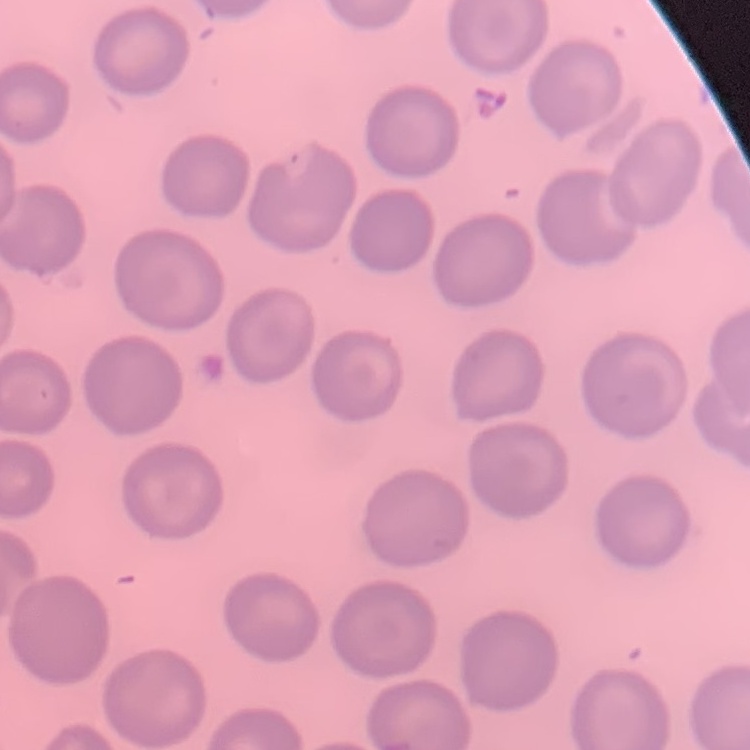

The red blood cells exhibit no rouleaux formation. Thin blood smear. Field's or Giemsa stain. Square crop of a larger photomicrograph.